Report the malaria status of this cell.
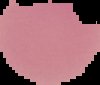
Uninfected.

{
  "image_type": "segmented cell region with the area outside set to black",
  "preparation": "thin blood smear",
  "image_size": "100×85 pixels"
}